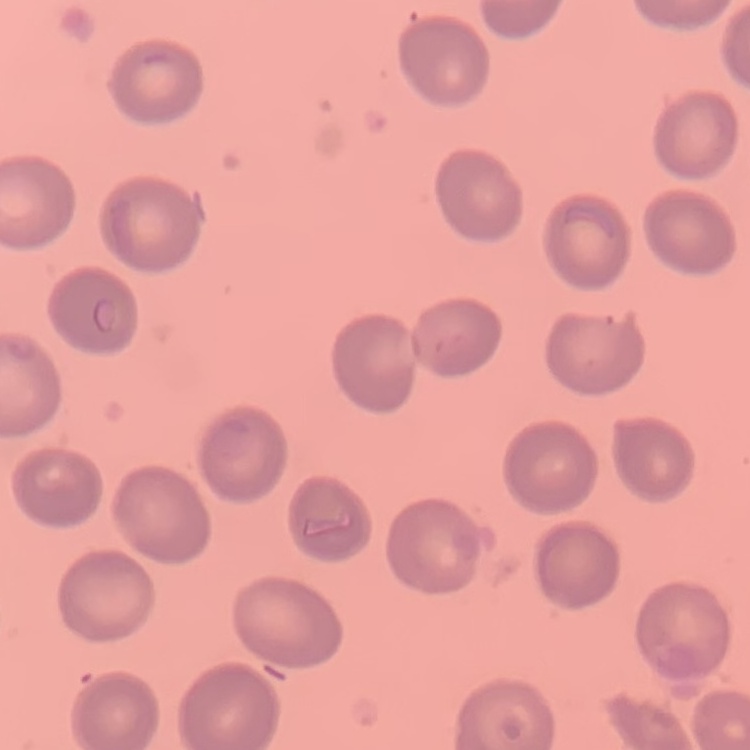 The erythrocytes show no rouleaux formation. One tile cut from a larger photomicrograph. Thin blood smear. Stained with either Field's or Giemsa.